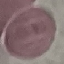

Summary:
  - Result: no malaria parasites detected
  - Stain: Giemsa
  - Capture: smartphone through the microscope eyepiece
  - Preparation: thin smear
  - Image type: cell patch, automatically extracted from a larger field of view and resized to 64 × 64 pixels